State which cell type is depicted.
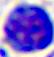
A leukocyte.

Micrograph. Captured at 400x magnification.